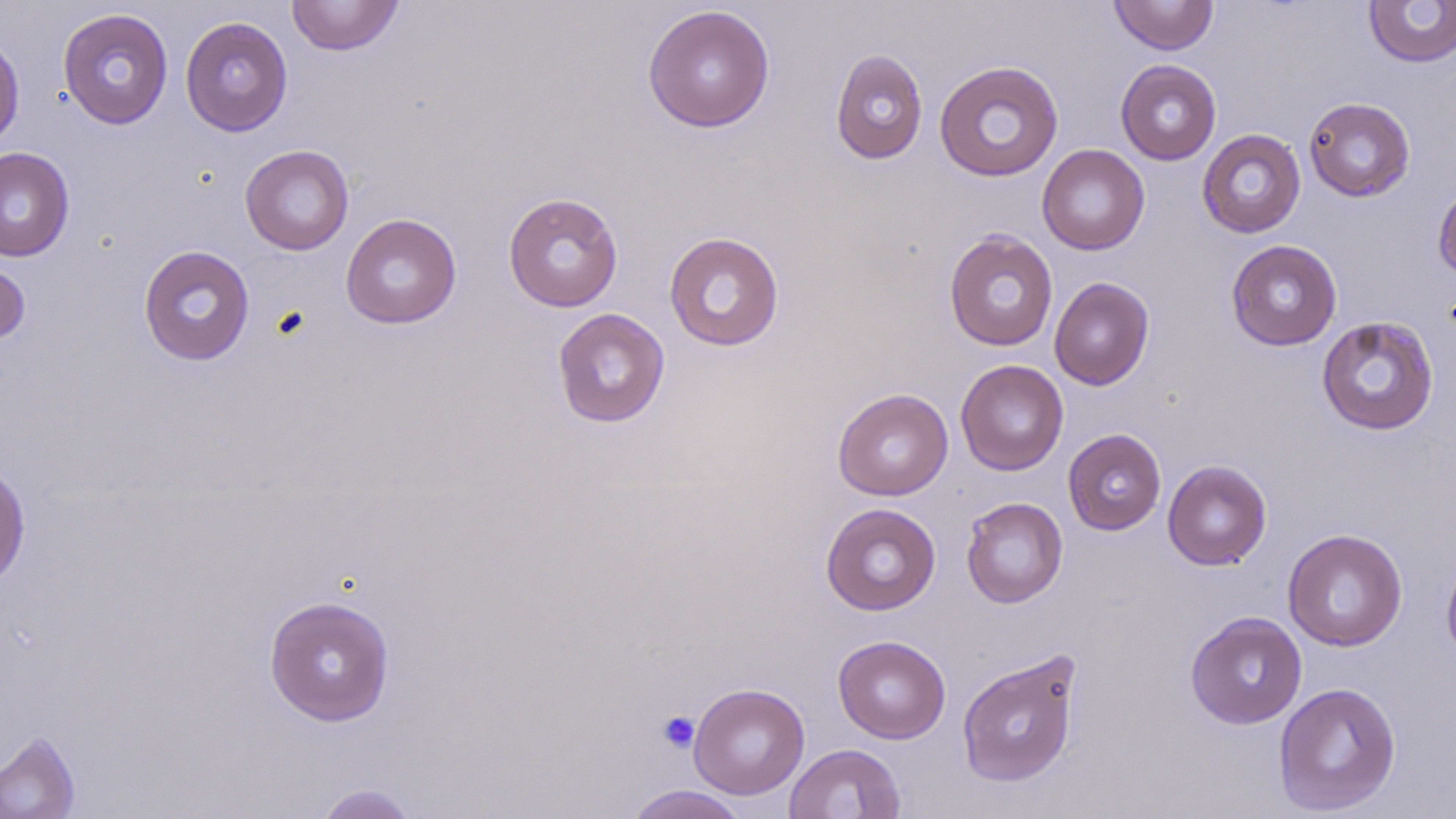

{
  "slide_level_diagnosis": "negative for blood parasites",
  "magnification": "1000x",
  "image_size": "1456×819 pixels",
  "platelet_locations": "approximate bounding boxes as (x1,y1)-(x2,y2) corner pairs in pixels: (657,710)-(699,753)",
  "stain": "May-Grünwald-Giemsa",
  "preparation": "thin blood film",
  "modality": "light microscopy",
  "field_of_view": "one of a larger specimen",
  "uninfected_red_blood_cell_locations": "approximate bounding boxes as (x1,y1)-(x2,y2) corner pairs in pixels: (286,0)-(404,56), (1108,0)-(1219,55), (1363,1)-(1456,68), (642,4)-(775,133), (58,7)-(173,130), (180,16)-(293,136), (0,31)-(25,153), (830,49)-(928,165), (1115,59)-(1222,165), (934,60)-(1064,182), (1303,97)-(1416,202), (1197,129)-(1306,238), (240,144)-(354,255), (1037,144)-(1150,255), (0,147)-(75,262), (1432,181)-(1456,283), (503,192)-(623,313), (340,213)-(462,329), (943,229)-(1059,351), (664,231)-(785,352), (1226,239)-(1342,351), (138,244)-(255,366), (0,258)-(30,346), (1049,276)-(1155,390), (551,308)-(670,428), (1315,315)-(1439,436), (955,359)-(1069,476), (832,388)-(953,501), (1063,429)-(1166,535), (1162,460)-(1272,570), (0,461)-(31,589), (961,497)-(1068,608), (821,502)-(941,615), (1282,528)-(1408,652), (1440,548)-(1456,669), (263,595)-(396,726), (1185,611)-(1307,729), (833,635)-(950,744), (956,650)-(1082,789), (1273,681)-(1402,816), (688,683)-(809,800), (0,730)-(81,819), (783,743)-(905,819), (313,783)-(420,819), (624,785)-(750,819)"
}